Assess the morphology of the red blood cells.
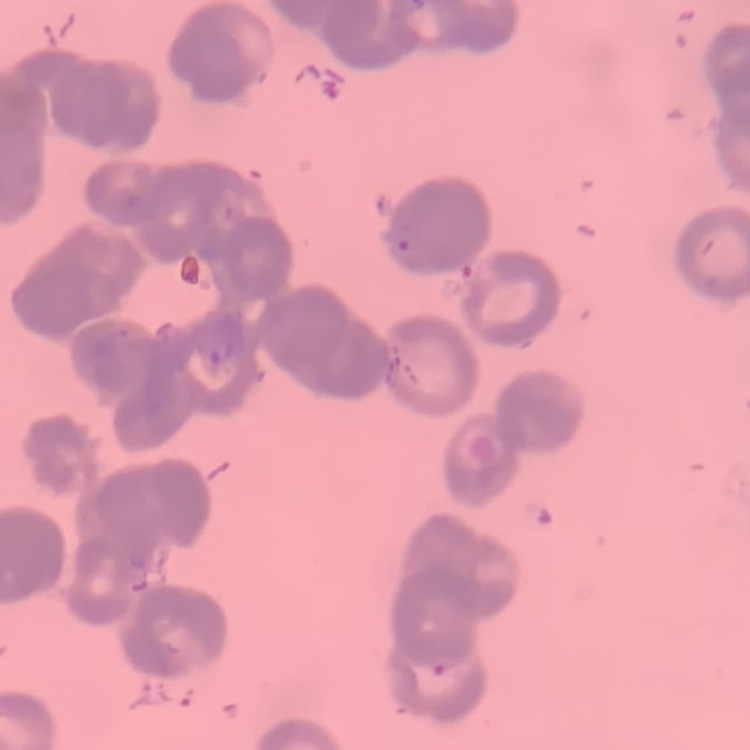

They show rouleaux formation.

One tile cut from a larger photomicrograph. Stained with either Field's or Giemsa. Thin blood film.